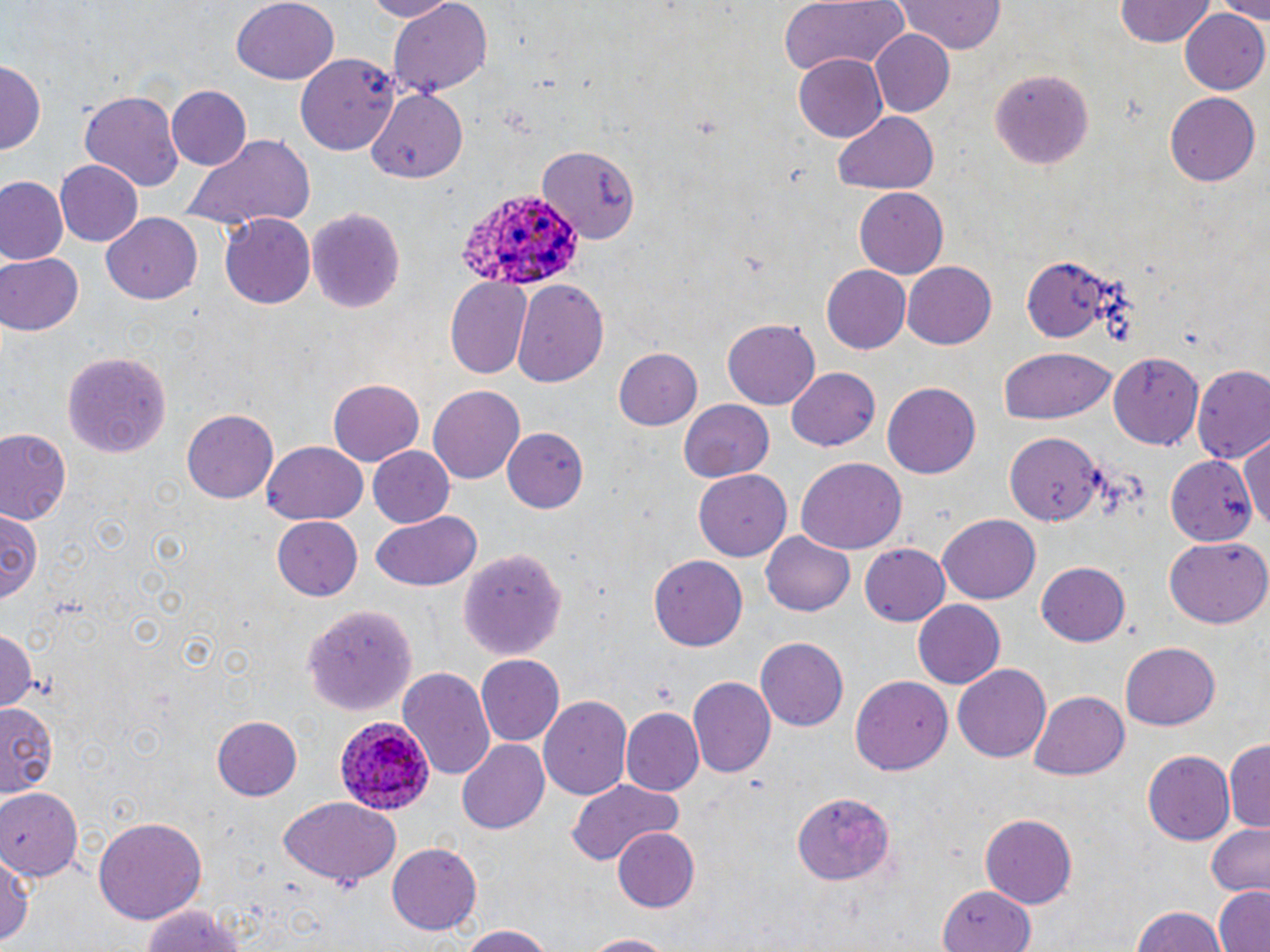

Summary:
  - Coordinate format: approximate bounding boxes as (x1,y1)-(x2,y2) corner pairs in pixels
  - Plasmodium ovale-infected red blood cell locations: (454,189)-(580,288), (336,716)-(436,816)
  - Uninfected red blood cell locations: (356,0)-(457,21), (780,0)-(910,73), (894,0)-(1010,56), (1115,0)-(1216,47), (1211,0)-(1270,22), (231,1)-(339,86), (388,1)-(491,95), (1180,8)-(1270,95), (868,28)-(956,117), (295,52)-(403,153), (794,54)-(889,142), (0,59)-(43,157), (987,67)-(1093,171), (167,84)-(251,170), (363,84)-(470,186), (80,90)-(185,194), (1165,92)-(1260,186), (831,108)-(939,194), (183,134)-(314,225), (536,144)-(639,241), (54,159)-(145,246), (0,176)-(67,264), (853,188)-(947,278), (308,205)-(406,316), (101,213)-(201,305), (220,213)-(316,308), (0,253)-(82,337), (1021,259)-(1125,342), (903,262)-(996,348), (820,265)-(910,354), (444,279)-(532,380), (513,279)-(610,388), (722,319)-(819,410), (998,347)-(1115,425), (613,348)-(704,430), (65,351)-(170,456), (1110,353)-(1201,451), (1192,366)-(1270,466), (786,367)-(880,452), (327,380)-(424,466), (882,382)-(981,478), (429,384)-(525,483), (680,399)-(773,482), (182,410)-(278,504), (504,427)-(588,512), (1,429)-(71,522), (1006,432)-(1104,526), (1241,438)-(1270,528), (262,441)-(368,525), (367,447)-(456,530), (1166,454)-(1259,546), (795,458)-(906,557), (693,470)-(792,559), (0,505)-(41,603), (370,512)-(480,592), (936,514)-(1041,604), (272,517)-(363,601), (761,530)-(856,618), (1163,539)-(1269,629), (860,543)-(951,627), (460,547)-(568,660), (647,553)-(748,652), (1037,561)-(1132,647), (912,600)-(1006,689), (304,601)-(419,715), (0,624)-(38,714), (755,637)-(847,731), (1118,643)-(1218,731), (475,654)-(565,747), (954,665)-(1050,761), (397,666)-(497,782), (851,672)-(950,776), (689,677)-(775,777), (1028,690)-(1132,781), (539,696)-(632,798), (0,704)-(59,795), (619,708)-(702,793), (211,714)-(303,800), (455,739)-(549,836), (1225,742)-(1270,834), (1143,750)-(1233,844), (565,781)-(683,864), (0,787)-(85,881), (794,790)-(897,883), (279,797)-(403,885), (980,814)-(1077,907), (93,816)-(207,926), (1206,822)-(1270,895), (612,827)-(702,914), (387,843)-(483,935), (0,848)-(31,950), (938,884)-(1039,952), (1213,885)-(1270,952), (137,902)-(252,952), (1127,905)-(1231,952), (451,923)-(559,952), (574,932)-(683,951)
  - Slide-level diagnosis: Plasmodium ovale
  - Magnification: 1000x
  - Modality: optical microscopy
  - Stain: May-Grünwald-Giemsa
  - Image size: 1270×952 pixels
  - Preparation: thin blood smear
  - Field of view: single